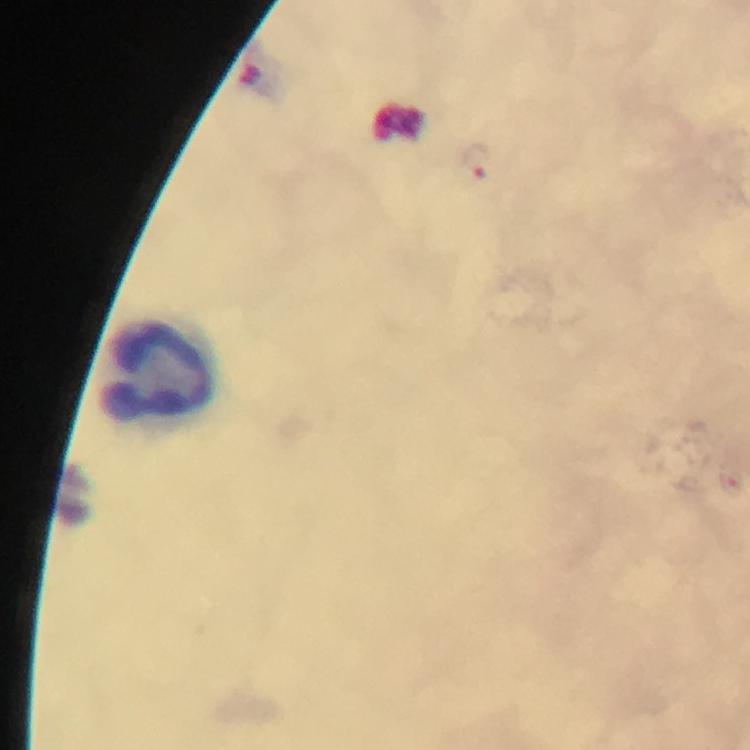

Approximate centers as {x, y} in pixels. Leukocyte locations: {160, 369}. Plasmodium parasite locations: {478, 160}. Photographed with a smartphone mounted on the microscope. Thick blood smear. 100x magnification. From a malaria diagnostic workup. Giemsa stain. Immersion oil was used. Cropped region of a single field of view. Image is 750×750 pixels.